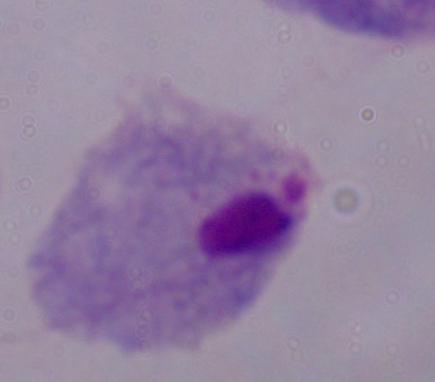

Micrograph. A trichomonad is seen. Captured at 1000x magnification.